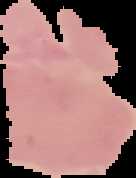 Image is 136×178 pixels. Cell region segmented out of the field of view; the surrounding area is masked to black. From a thin blood film. Malaria status: uninfected.